Classify this cell by malaria status.
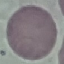
It is uninfected.

Cell patch, automatically extracted from a larger field of view and resized to 64 × 64 pixels. Giemsa-stained preparation. Thin smear of blood. Photographed with a smartphone camera at the microscope eyepiece.